Name the blood parasite species.
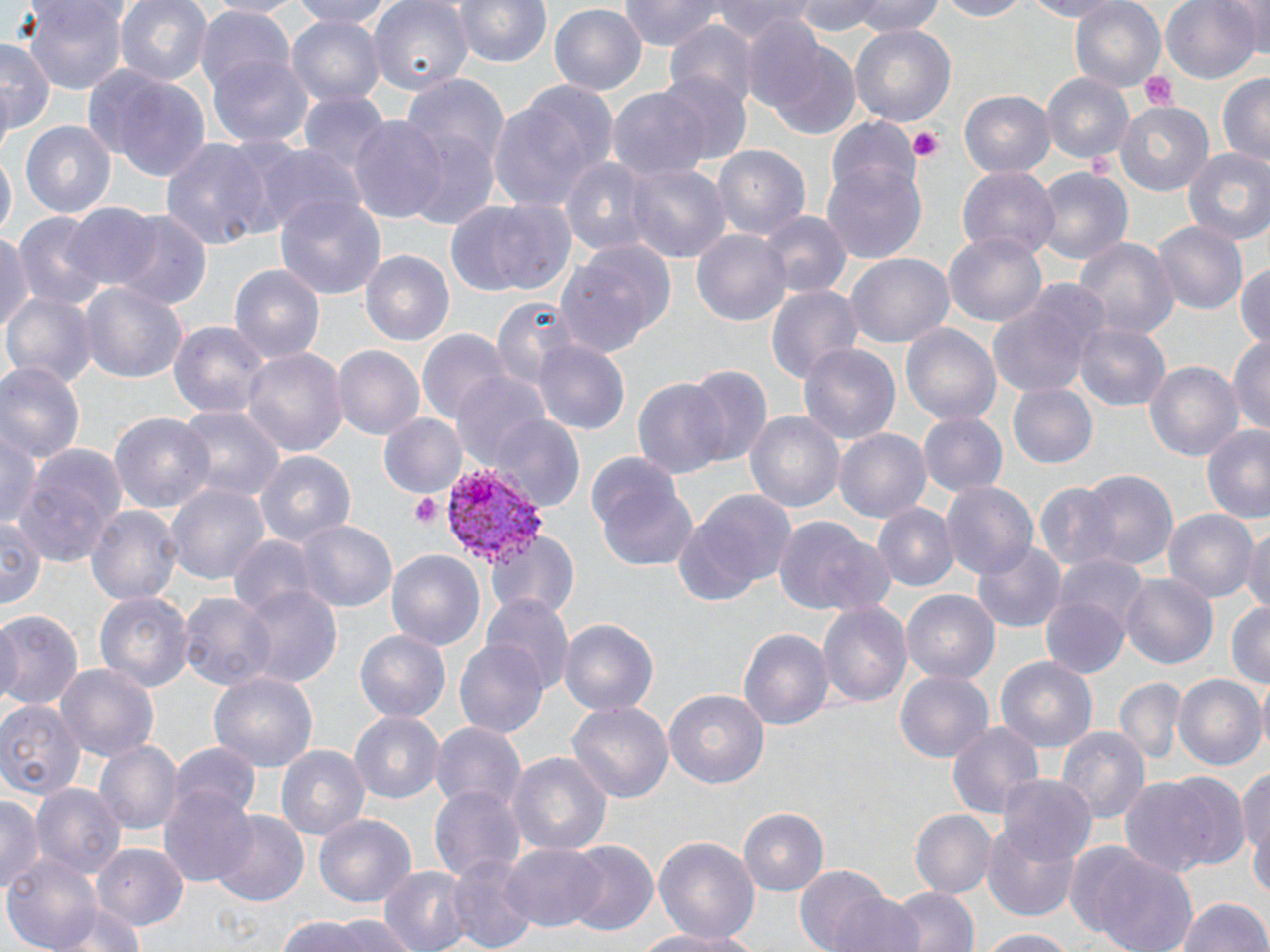

Plasmodium vivax.

Summary:
  - Coordinate format: approximate bounding boxes as (x1, y1, x2, y2) in pixels
  - Uninfected red blood cell locations: (25, 0, 126, 94), (114, 0, 214, 89), (211, 0, 307, 18), (285, 0, 399, 27), (368, 0, 472, 95), (452, 0, 553, 67), (618, 0, 722, 49), (709, 0, 814, 43), (796, 0, 898, 37), (845, 0, 944, 37), (928, 0, 1032, 21), (1012, 0, 1127, 22), (1070, 0, 1166, 91), (1161, 0, 1263, 86), (1226, 0, 1268, 56), (548, 3, 646, 93), (196, 6, 296, 100), (739, 13, 840, 124), (286, 17, 385, 105), (663, 20, 753, 108), (847, 25, 957, 131), (0, 38, 53, 143), (767, 43, 863, 143), (207, 55, 313, 148), (96, 70, 212, 180), (658, 70, 750, 164), (1216, 73, 1270, 166), (401, 74, 508, 171), (1041, 74, 1133, 165), (607, 86, 713, 182), (298, 90, 389, 180), (959, 90, 1055, 180), (482, 92, 607, 216), (1115, 101, 1213, 198), (352, 116, 447, 223), (21, 122, 116, 220), (403, 129, 499, 231), (161, 139, 272, 250), (708, 143, 810, 243), (256, 144, 361, 233), (822, 147, 928, 262), (1183, 147, 1270, 248), (0, 153, 14, 245), (560, 156, 659, 257), (625, 161, 730, 265), (957, 167, 1060, 263), (1035, 168, 1132, 270), (276, 192, 386, 300), (453, 197, 579, 299), (64, 204, 160, 289), (759, 210, 851, 299), (114, 213, 212, 312), (13, 216, 107, 312), (1152, 219, 1247, 317), (0, 224, 30, 339), (692, 228, 791, 328), (943, 230, 1047, 329), (1073, 236, 1178, 343), (556, 237, 676, 351), (360, 251, 455, 350), (845, 254, 955, 348), (1234, 261, 1270, 348), (230, 264, 325, 365), (78, 281, 190, 385), (766, 285, 861, 386), (983, 290, 1102, 402), (6, 292, 95, 386), (490, 297, 582, 390), (166, 320, 275, 421), (1073, 320, 1171, 411), (899, 322, 1002, 428), (417, 330, 510, 420), (1228, 338, 1270, 434), (533, 340, 628, 436), (797, 342, 900, 446), (333, 346, 425, 443), (241, 347, 346, 458), (1191, 350, 1267, 451), (1143, 361, 1243, 462), (0, 362, 85, 462), (679, 365, 772, 470), (453, 372, 553, 470), (631, 376, 729, 479), (1007, 383, 1099, 470), (178, 407, 282, 509), (109, 411, 217, 513), (745, 411, 843, 512), (917, 411, 1008, 498), (376, 414, 467, 500), (490, 415, 583, 509), (834, 425, 931, 522), (1199, 425, 1270, 525), (1, 427, 40, 531), (15, 445, 126, 566), (255, 451, 356, 551), (586, 453, 698, 572), (1079, 470, 1177, 572), (941, 481, 1038, 585), (165, 482, 270, 589), (1033, 482, 1120, 575), (680, 488, 801, 604), (86, 501, 182, 605), (872, 503, 958, 594), (1162, 506, 1258, 600), (1, 516, 44, 611), (770, 516, 889, 618), (293, 517, 398, 616), (1244, 522, 1270, 619), (486, 528, 582, 621), (228, 536, 320, 622), (975, 542, 1065, 631), (387, 550, 485, 654), (1055, 556, 1150, 640), (1119, 573, 1218, 670), (238, 582, 343, 687), (899, 587, 999, 683), (95, 591, 193, 695), (180, 593, 276, 693), (1043, 594, 1128, 677), (483, 596, 574, 698), (817, 600, 912, 706), (1226, 602, 1270, 691), (0, 609, 86, 713), (558, 616, 660, 714), (738, 627, 834, 735), (355, 629, 451, 725), (453, 638, 548, 739), (995, 655, 1099, 755), (55, 664, 159, 761), (895, 668, 993, 763), (208, 672, 317, 773), (1174, 673, 1266, 772), (1113, 678, 1186, 766), (664, 689, 769, 791), (0, 696, 85, 802), (568, 701, 672, 805), (351, 710, 446, 804), (429, 721, 527, 812), (946, 721, 1047, 824), (1057, 727, 1149, 826), (276, 741, 372, 839), (93, 742, 181, 836), (169, 744, 262, 821), (507, 750, 612, 862), (1239, 764, 1269, 893), (1129, 772, 1249, 875), (996, 775, 1100, 866), (429, 783, 526, 883), (0, 784, 88, 896), (160, 784, 259, 887), (30, 785, 124, 880), (1, 795, 44, 899), (739, 806, 829, 895), (213, 809, 309, 905), (911, 809, 996, 898), (316, 812, 417, 907), (979, 825, 1083, 924), (652, 835, 760, 942), (564, 842, 658, 937), (500, 843, 606, 931), (92, 844, 188, 929), (1067, 845, 1198, 952), (3, 852, 104, 952), (446, 856, 538, 949), (798, 864, 898, 952), (381, 865, 474, 952), (888, 887, 978, 952), (825, 893, 930, 952), (1173, 896, 1270, 952), (45, 898, 149, 952), (278, 913, 411, 952), (629, 929, 759, 952), (975, 929, 1080, 952)
  - Platelet locations: (1141, 70, 1181, 112), (908, 127, 944, 163), (409, 493, 444, 526)
  - Plasmodium vivax-infected red blood cell locations: (438, 461, 550, 566)
  - Stain: May-Grünwald-Giemsa
  - Preparation: thin blood smear
  - Field of view: single
  - Magnification: 1000x
  - Image size: 1270×952 pixels
  - Modality: optical microscopy